Report the malaria status of this cell.
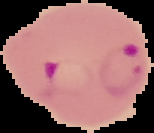
Parasitized.

image_size: 154×133 pixels
image_type: cell region segmented out of the field of view; surrounding area masked to black
preparation: thin blood film